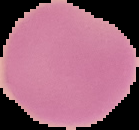
Summary:
  - Image size: 139×130 pixels
  - Preparation: thin blood film
  - Image type: segmented cell region on a black background
  - Malaria status: uninfected